Name the parasite shown.
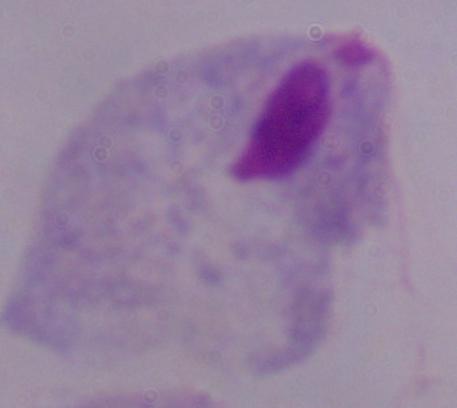
A trichomonad.

Summary:
  - Magnification: 1000x
  - Modality: micrograph